Give the extent of all uninfected red blood cells.
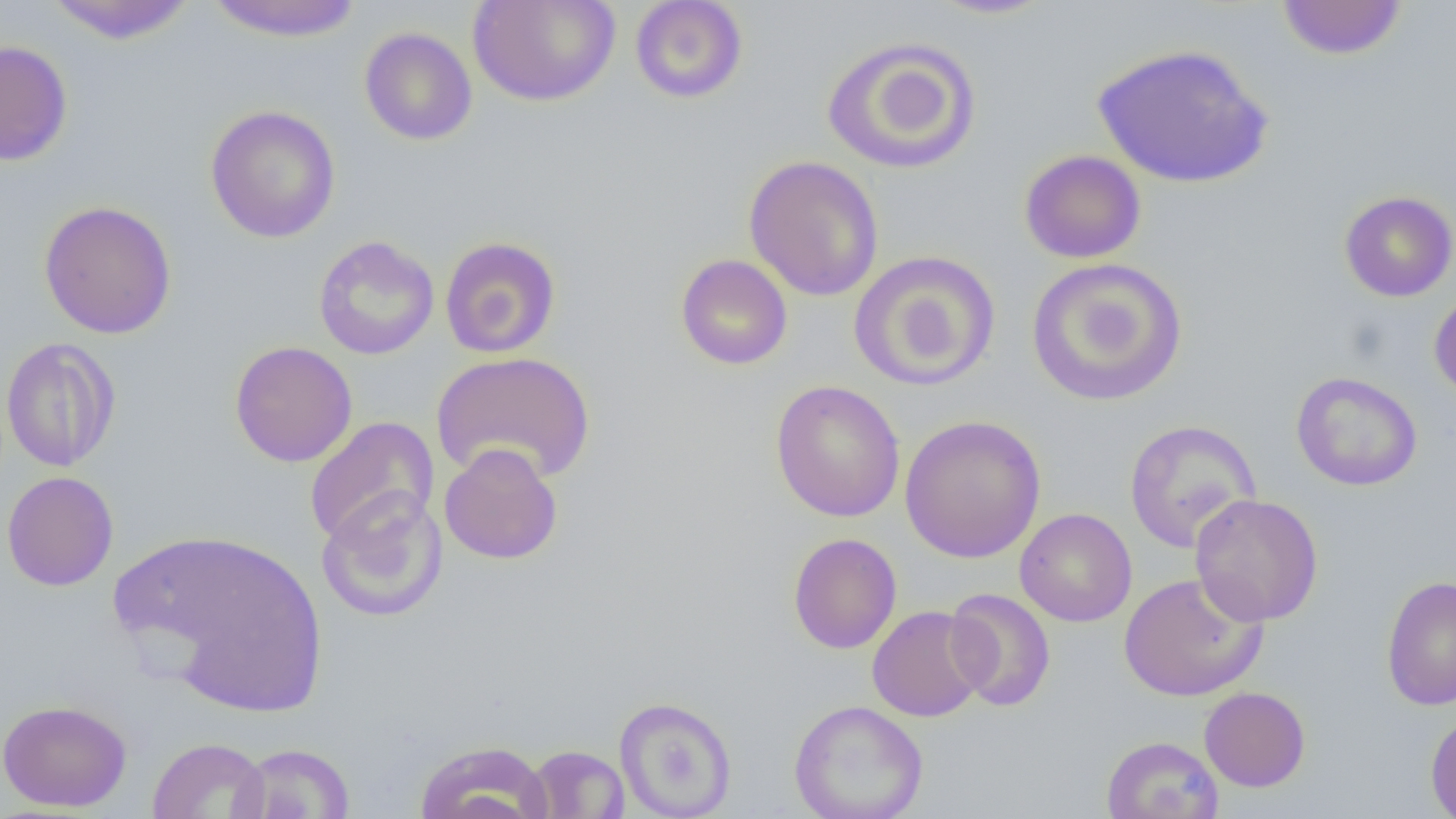

Approximate bounding boxes as (x1, y1, x2, y2) in pixels.
Uninfected red blood cells: (203, 0, 365, 42), (467, 0, 621, 107), (630, 0, 748, 104), (927, 0, 1057, 20), (1276, 0, 1408, 60), (44, 1, 199, 44), (358, 27, 478, 146), (821, 36, 981, 175), (0, 39, 73, 166), (1092, 42, 1274, 189), (205, 104, 341, 243), (1019, 149, 1147, 264), (743, 155, 884, 302), (1339, 190, 1456, 302), (38, 200, 176, 339), (313, 236, 439, 360), (439, 236, 561, 359), (848, 250, 1001, 392), (675, 253, 793, 370), (1025, 257, 1189, 406), (1429, 287, 1456, 402), (1, 337, 120, 472), (229, 340, 358, 467), (431, 350, 596, 485), (1291, 371, 1423, 491), (770, 379, 906, 522), (898, 414, 1047, 563), (304, 416, 440, 547), (1123, 419, 1261, 554), (439, 442, 563, 565), (2, 471, 119, 591), (316, 489, 448, 623), (1190, 493, 1324, 626), (1015, 508, 1137, 627), (117, 528, 329, 713), (788, 532, 902, 654), (1118, 572, 1268, 702), (1381, 576, 1456, 711), (944, 588, 1056, 711), (867, 605, 989, 723), (1199, 687, 1310, 792), (614, 695, 738, 818), (0, 699, 132, 811), (789, 699, 929, 819), (1425, 712, 1456, 818), (1101, 735, 1224, 819), (148, 737, 269, 819), (414, 739, 553, 819), (235, 743, 355, 819), (526, 744, 629, 818).

Summary:
  - Slide-level diagnosis: no evidence of blood parasites
  - Modality: optical microscopy
  - Field of view: single
  - Image size: 1456×819 pixels
  - Preparation: thin blood smear
  - Magnification: 1000x